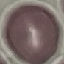

Result: negative for malaria parasites. Cell patch, automatically extracted from a larger field of view and resized to 64 × 64 pixels. Acquired by smartphone through the microscope eyepiece. Thin smear of blood. Giemsa stain.